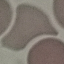
Summary:
  - Result: no malaria parasites detected
  - Capture: smartphone camera at the microscope eyepiece
  - Stain: Giemsa
  - Preparation: thin blood film
  - Image type: automatically extracted cell patch, resized to 64 × 64 pixels